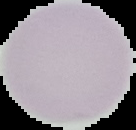
Cell region segmented out of the field of view; the surrounding area is masked to black. From a thin blood film. Image is 136×130 pixels. Malaria status: uninfected.